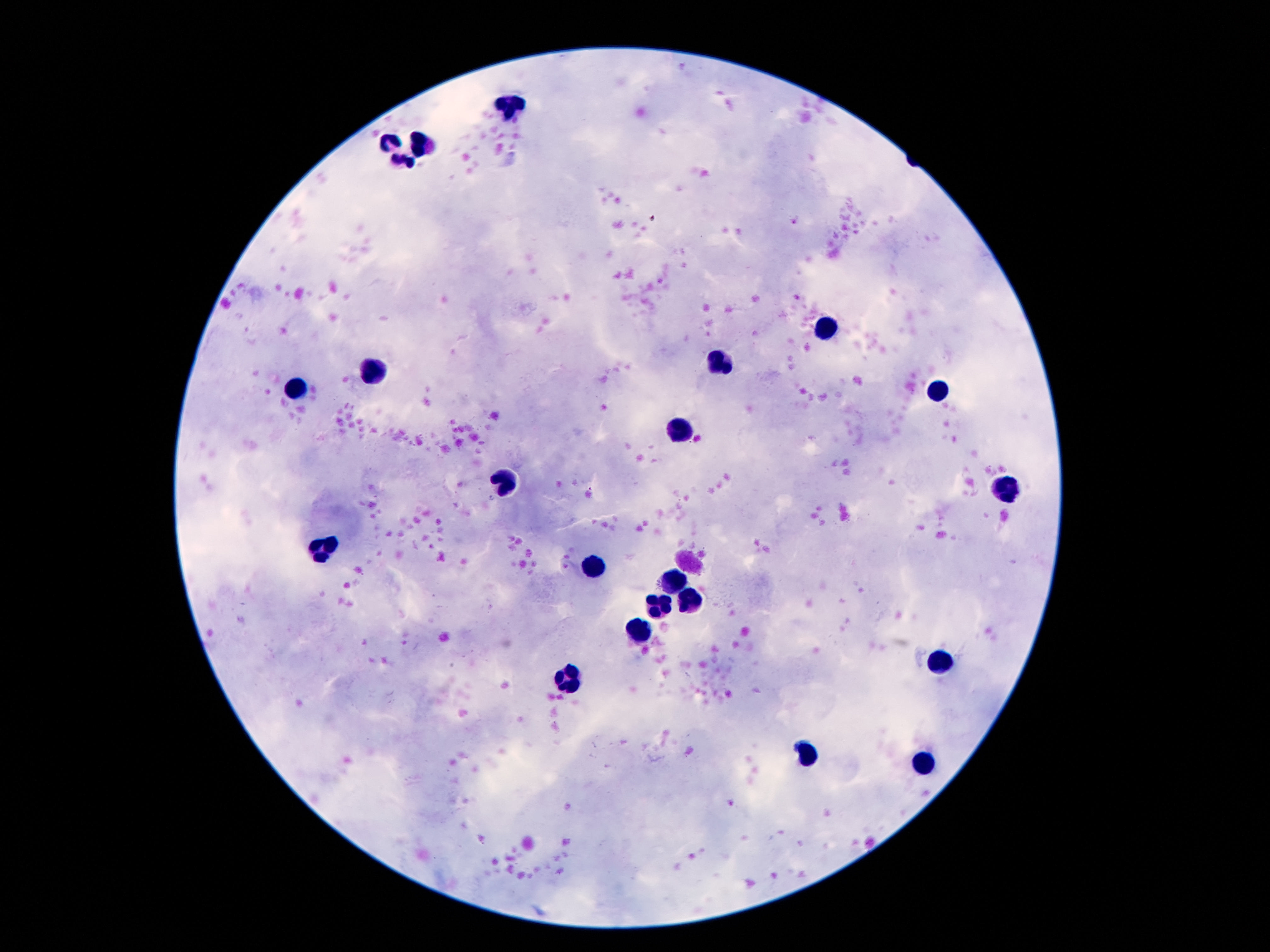
Approximate object centers, in pixels from the top-left corner. Leukocyte locations: (x=513, y=106), (x=391, y=142), (x=422, y=144), (x=403, y=160), (x=826, y=324), (x=725, y=363), (x=368, y=370), (x=298, y=388), (x=938, y=389), (x=679, y=431), (x=506, y=480), (x=1005, y=492), (x=324, y=545), (x=597, y=566), (x=676, y=582), (x=693, y=601), (x=662, y=610), (x=641, y=634), (x=938, y=661), (x=809, y=750), (x=921, y=763). Image is 1270×952 pixels. Single field of view. Thick peripheral-blood smear. 100x magnification. Giemsa stain. Photographed through the microscope eyepiece with a smartphone camera. Patient malaria status: uninfected.